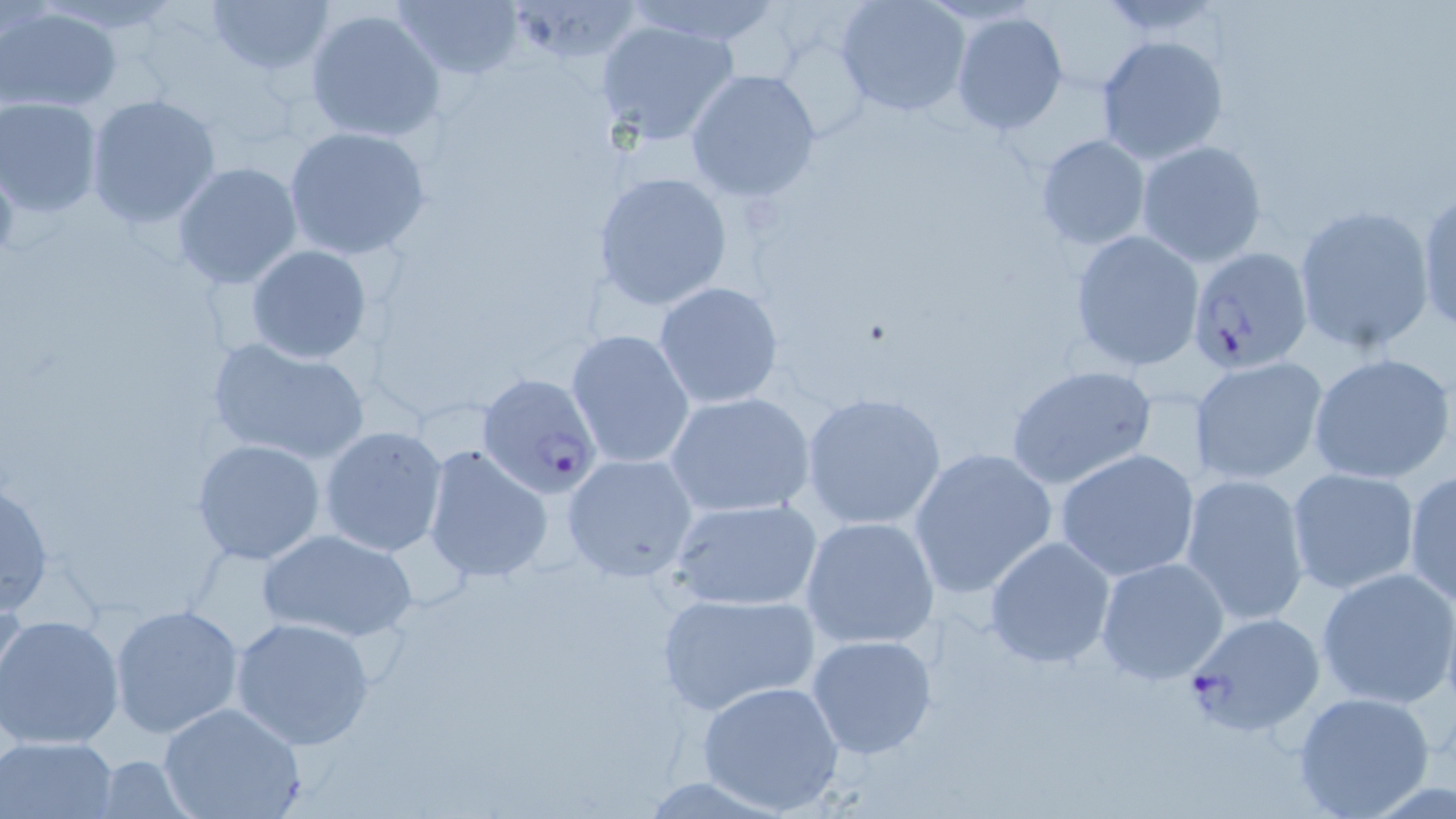
{
  "plasmodium_falciparum_infected_red_blood_cell_locations": "approximate bounding boxes as (x1, y1, x2, y2) in pixels: (1184, 247, 1311, 375), (476, 371, 605, 498), (1181, 611, 1327, 738)",
  "slide_level_diagnosis": "Plasmodium falciparum",
  "modality": "optical microscopy",
  "stain": "May-Grünwald-Giemsa",
  "uninfected_red_blood_cell_locations": "approximate bounding boxes as (x1, y1, x2, y2) in pixels: (205, 0, 337, 74), (394, 0, 526, 81), (628, 0, 784, 45), (833, 0, 970, 120), (516, 2, 647, 63), (0, 3, 123, 113), (303, 7, 446, 144), (949, 11, 1069, 135), (592, 17, 742, 147), (1095, 34, 1227, 165), (684, 69, 821, 202), (85, 93, 222, 230), (0, 97, 103, 217), (282, 125, 432, 261), (1034, 133, 1151, 250), (1135, 140, 1267, 267), (171, 163, 304, 289), (591, 170, 734, 311), (1415, 187, 1456, 335), (1294, 204, 1434, 355), (1068, 229, 1205, 372), (245, 245, 373, 364), (654, 281, 784, 409), (566, 329, 695, 470), (206, 335, 370, 465), (1307, 352, 1456, 487), (1190, 357, 1327, 486), (1004, 364, 1155, 491), (801, 390, 948, 531), (664, 392, 816, 520), (319, 425, 450, 558), (192, 439, 326, 566), (423, 443, 553, 583), (906, 447, 1058, 599), (1054, 448, 1203, 582), (560, 453, 700, 582), (1285, 466, 1420, 596), (1404, 469, 1455, 607), (1181, 473, 1311, 628), (0, 477, 54, 618), (667, 498, 823, 610), (799, 516, 942, 650), (258, 528, 417, 643), (983, 536, 1117, 670), (1095, 556, 1231, 686), (1316, 565, 1456, 710), (0, 571, 27, 710), (655, 588, 819, 717), (109, 603, 245, 741), (0, 613, 127, 748), (229, 615, 377, 750), (805, 633, 940, 761), (698, 681, 847, 815), (1292, 691, 1437, 817), (157, 701, 308, 819), (2, 735, 119, 818)",
  "magnification": "1000x",
  "field_of_view": "one of a larger specimen",
  "preparation": "thin blood smear",
  "image_size": "1456×819 pixels"
}